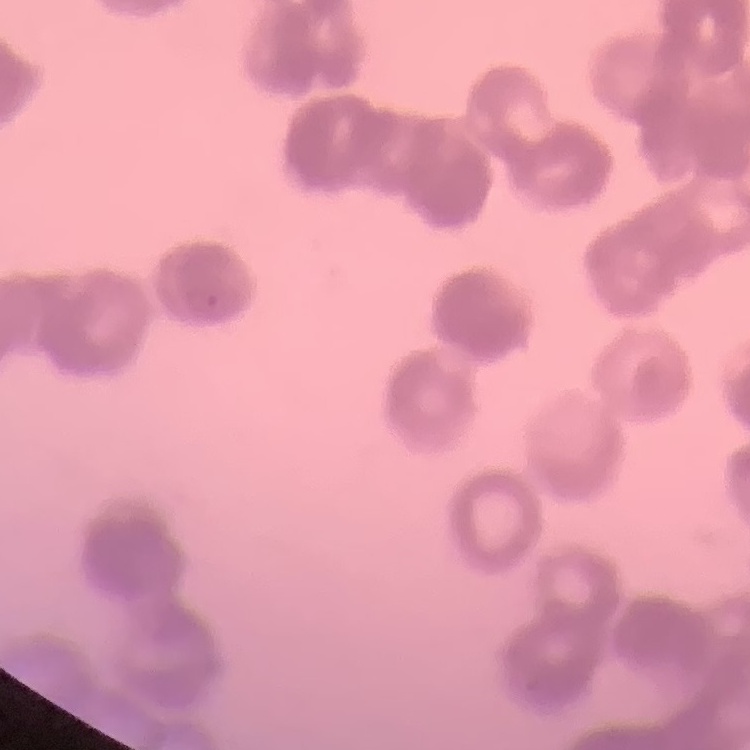
Summary:
  - Erythrocyte morphology: rouleaux formation
  - Preparation: thin peripheral smear
  - Stain: Field's or Giemsa
  - Image type: one tile cut from a larger photomicrograph